Locate every blood parasite and identify its species.
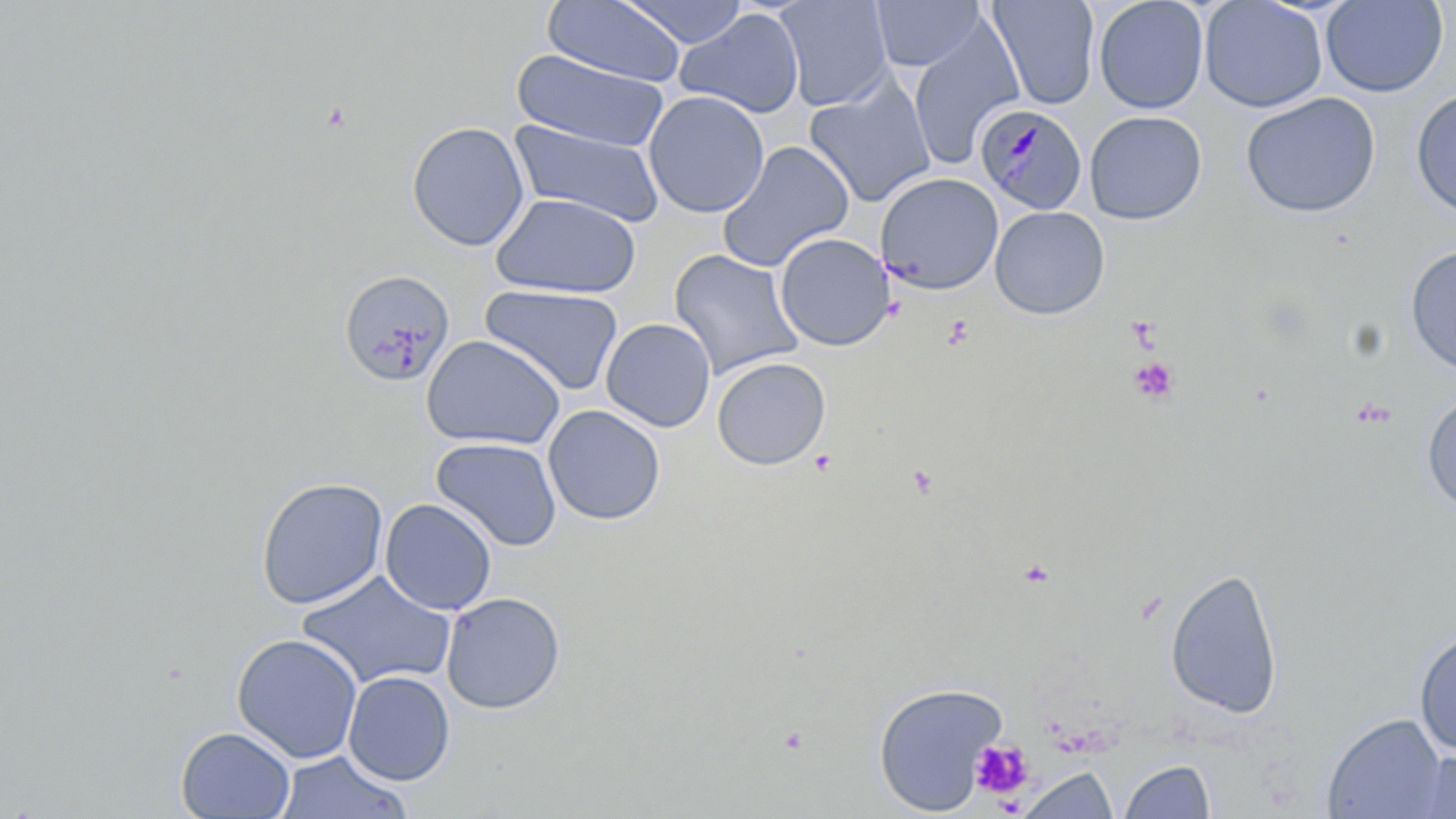
Approximate bounding boxes as [x1, y1, x2, y2] in pixels.
Plasmodium malariae-infected red blood cells: [976, 103, 1089, 215].
No Plasmodium falciparum, Plasmodium ovale, Plasmodium vivax, Babesia divergens, or Trypanosoma brucei observed.

Summary:
  - Platelet locations: [1130, 357, 1179, 404], [969, 739, 1033, 800]
  - Uninfected red blood cell locations: [543, 0, 686, 87], [620, 0, 749, 48], [774, 0, 894, 111], [870, 0, 986, 71], [987, 0, 1100, 110], [1093, 0, 1209, 114], [1198, 0, 1328, 113], [1321, 0, 1448, 97], [674, 8, 805, 119], [907, 25, 1026, 172], [511, 49, 671, 154], [804, 75, 937, 207], [1411, 87, 1456, 219], [643, 90, 769, 218], [1241, 92, 1381, 217], [1084, 110, 1207, 225], [510, 118, 664, 230], [407, 122, 530, 251], [716, 141, 854, 272], [876, 172, 1004, 294], [490, 192, 641, 299], [990, 205, 1110, 320], [774, 233, 895, 351], [1405, 246, 1456, 376], [668, 249, 805, 380], [339, 269, 454, 387], [480, 284, 625, 396], [601, 318, 716, 432], [421, 334, 565, 450], [711, 357, 831, 470], [1422, 392, 1456, 514], [542, 405, 665, 525], [432, 437, 562, 551], [255, 476, 389, 609], [380, 498, 497, 615], [1165, 567, 1284, 719], [295, 571, 457, 692], [441, 591, 565, 714], [1414, 628, 1456, 755], [231, 633, 363, 764], [343, 670, 455, 785], [872, 681, 1008, 815], [1322, 713, 1450, 819], [175, 726, 296, 818], [1407, 749, 1456, 819], [273, 750, 412, 819], [1118, 759, 1217, 819], [1016, 765, 1118, 819]
  - Slide-level diagnosis: Plasmodium malariae
  - Stain: May-Grünwald-Giemsa
  - Field of view: one of a larger specimen
  - Image size: 1456×819 pixels
  - Preparation: thin blood film
  - Modality: optical microscopy
  - Magnification: 1000x